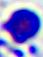 A white blood cell is seen. Photomicrograph. Captured at 400x magnification.